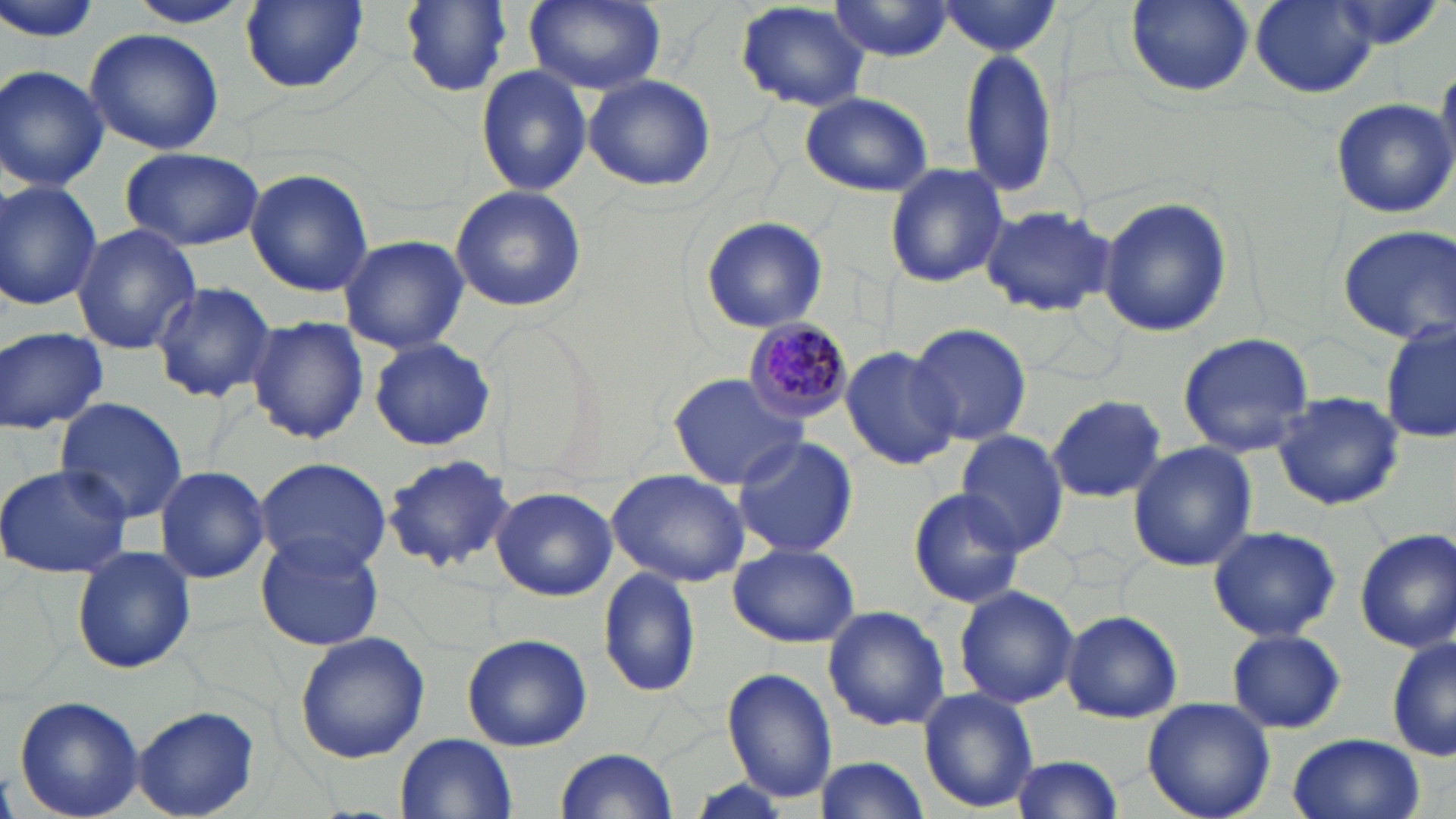

slide-level diagnosis = Plasmodium malariae
image size = 1456×819 pixels
uninfected red blood cell locations = approximate bounding boxes as [x1, y1, x2, y2] in pixels: [0, 0, 106, 45], [124, 0, 253, 28], [239, 0, 368, 93], [400, 0, 514, 95], [524, 0, 665, 95], [1125, 0, 1254, 96], [1251, 0, 1379, 98], [825, 1, 958, 63], [734, 2, 873, 113], [933, 2, 1065, 57], [82, 28, 225, 157], [957, 45, 1059, 198], [0, 65, 110, 192], [476, 65, 592, 196], [583, 73, 714, 192], [799, 90, 933, 196], [1329, 97, 1455, 217], [120, 147, 264, 252], [881, 161, 1009, 287], [244, 167, 373, 297], [0, 180, 103, 312], [449, 185, 587, 314], [1097, 195, 1234, 338], [978, 206, 1116, 317], [698, 214, 829, 335], [71, 224, 201, 356], [1336, 224, 1456, 345], [337, 234, 469, 354], [150, 279, 277, 402], [246, 315, 370, 444], [1381, 320, 1455, 448], [909, 321, 1032, 448], [0, 326, 107, 433], [1176, 332, 1316, 458], [368, 336, 496, 451], [840, 345, 960, 470], [669, 372, 808, 492], [1272, 391, 1404, 511], [1047, 394, 1167, 501], [53, 397, 189, 524], [954, 433, 1068, 553], [730, 434, 858, 560], [1126, 443, 1257, 573], [382, 453, 514, 573], [253, 457, 393, 576], [0, 463, 131, 579], [151, 467, 269, 583], [606, 468, 751, 587], [491, 486, 618, 599], [906, 487, 1028, 607], [1206, 523, 1342, 642], [1354, 529, 1456, 653], [255, 532, 383, 651], [728, 543, 860, 648], [72, 544, 197, 675], [597, 567, 701, 699], [953, 585, 1079, 710], [821, 605, 951, 731], [1061, 609, 1184, 723], [1225, 629, 1347, 734], [293, 632, 430, 763], [461, 633, 591, 752], [1388, 634, 1455, 764], [722, 668, 839, 801], [917, 687, 1039, 813], [12, 696, 145, 819], [1142, 697, 1278, 819], [131, 708, 261, 818], [396, 733, 515, 817], [1285, 733, 1424, 819], [554, 748, 680, 819], [1008, 753, 1125, 817], [810, 755, 932, 819]
magnification = 1000x
stain = May-Grünwald-Giemsa
field of view = one of a larger specimen
preparation = thin blood smear
modality = light microscopy
Plasmodium malariae-infected red blood cell locations = approximate bounding boxes as [x1, y1, x2, y2] in pixels: [740, 316, 854, 423]